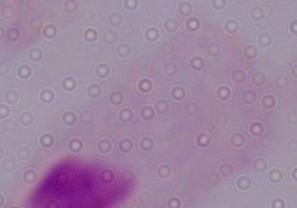
Summary:
  - Magnification: 1000x
  - Identification: trichomonad
  - Modality: photomicrograph